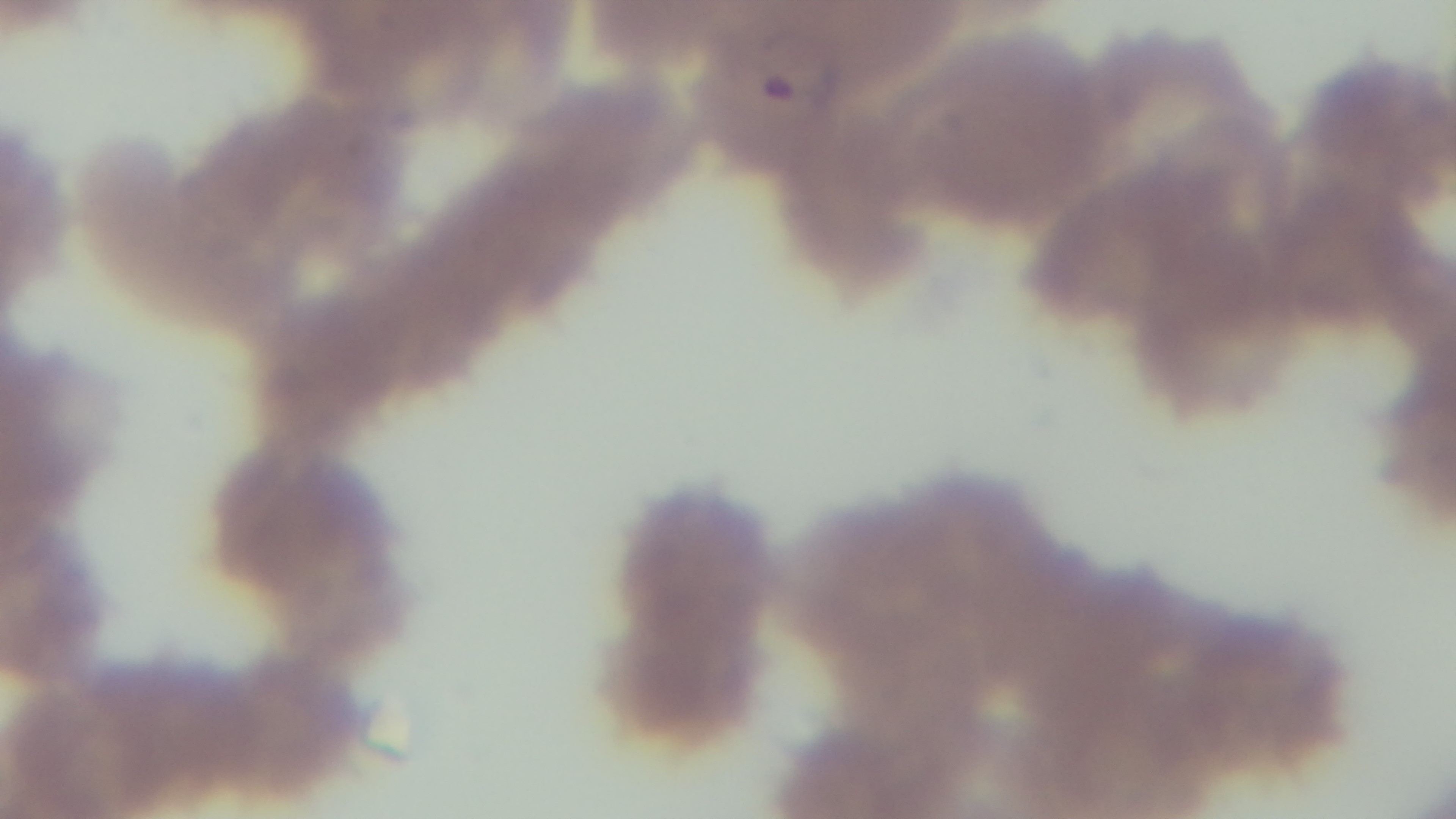
capture = mounted 4K digital camera
preparation = thin smear
malaria status = positive
field of view = single
objective = 100x oil immersion
stain = Giemsa
modality = light microscopy